Locate every Plasmodium parasite.
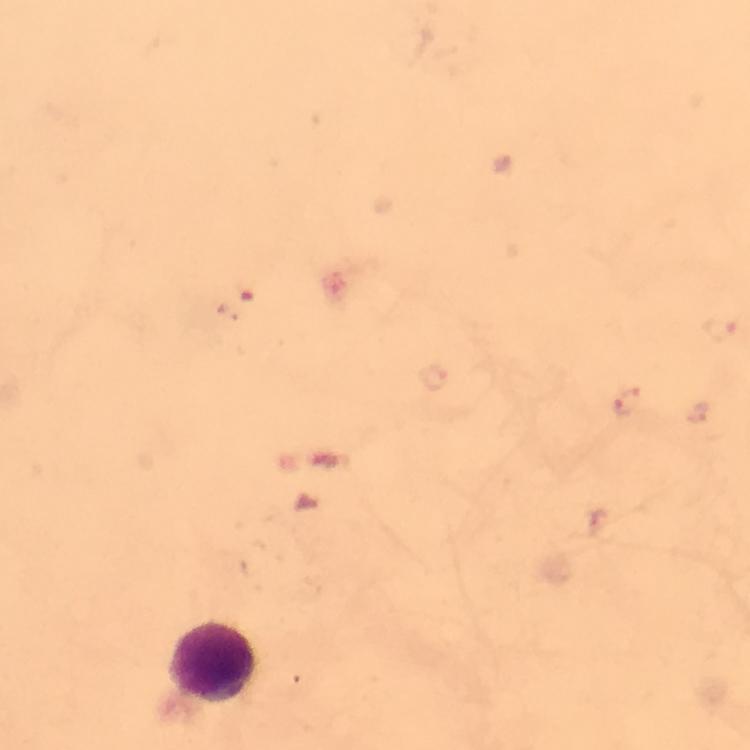

Approximate object centers, in pixels from the top-left corner.
Plasmodium parasites: (x=239, y=300), (x=719, y=327), (x=626, y=404).

Leukocyte locations: (x=212, y=665). Giemsa stain. Image is 750×750 pixels. Photographed through the microscope with a smartphone camera. From a diagnostic examination for malaria. Immersion oil was used. At 100x magnification. A crop from one field of view. Thick blood film.